Assess the morphology of the red blood cells.
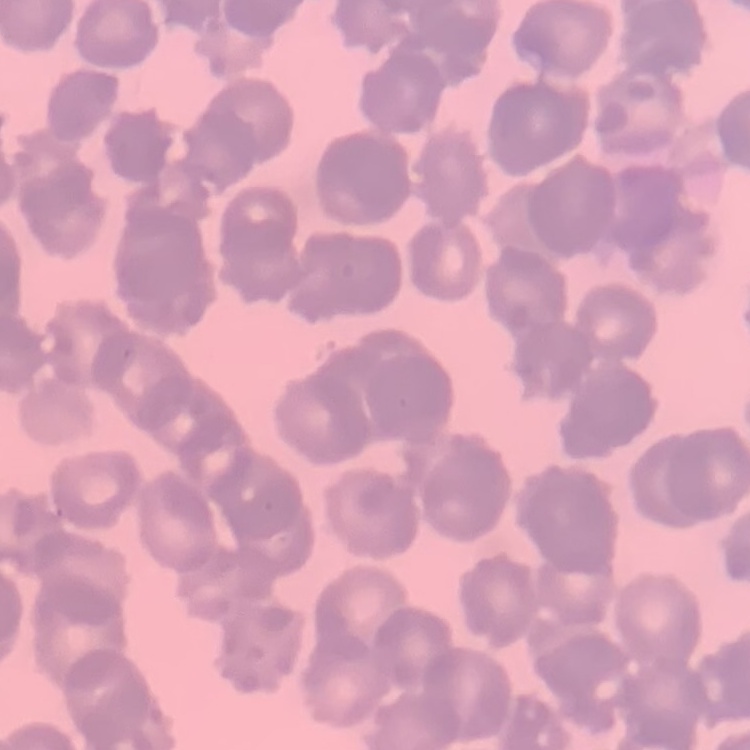

Rouleaux formation.

stain: Field's or Giemsa
image_type: square crop of a larger photomicrograph
preparation: thin blood film